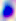

identification = Toxoplasma gondii
modality = micrograph
magnification = 400x